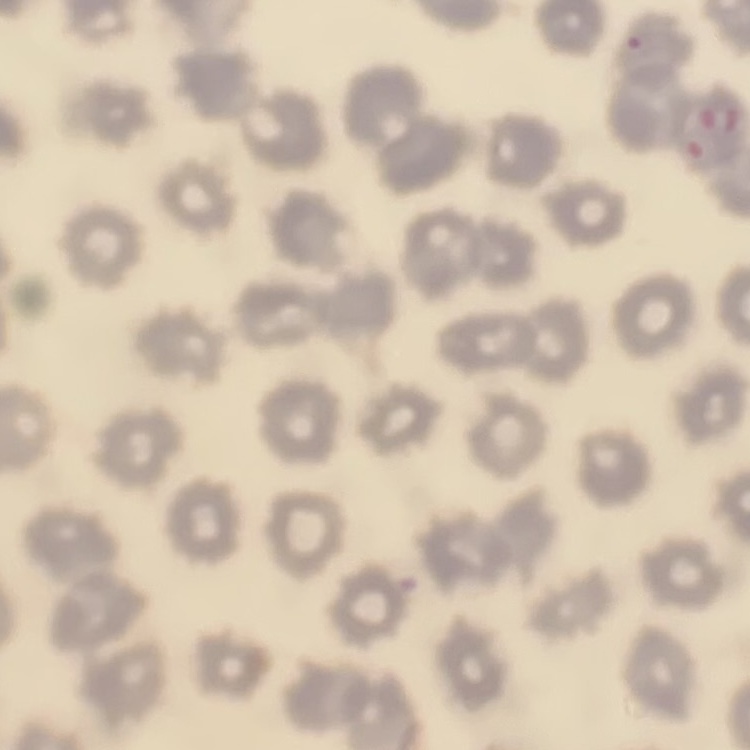
Summary:
  - Red blood cell morphology: no rouleaux formation
  - Stain: Field's or Giemsa
  - Preparation: thin peripheral smear
  - Image type: one tile cut from a larger photomicrograph